Classify this cell by malaria status.
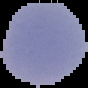
It is parasitized.

{
  "image_size": "88×88 pixels",
  "preparation": "thin blood smear",
  "image_type": "segmented cell region on a black background"
}